State which parasite is depicted.
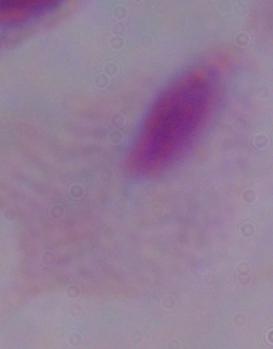
This is a trichomonad.

Captured at 1000x magnification. Micrograph.